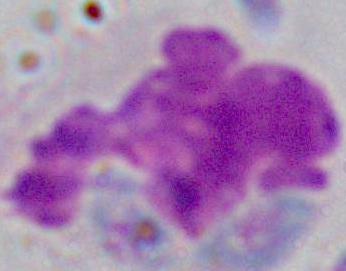 Captured at 1000x magnification. A leukocyte is shown. Photomicrograph.